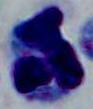
magnification = 1000x
identification = white blood cell
modality = micrograph